Name the parasite shown.
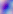

This is Toxoplasma gondii.

Photomicrograph. 400x magnification.